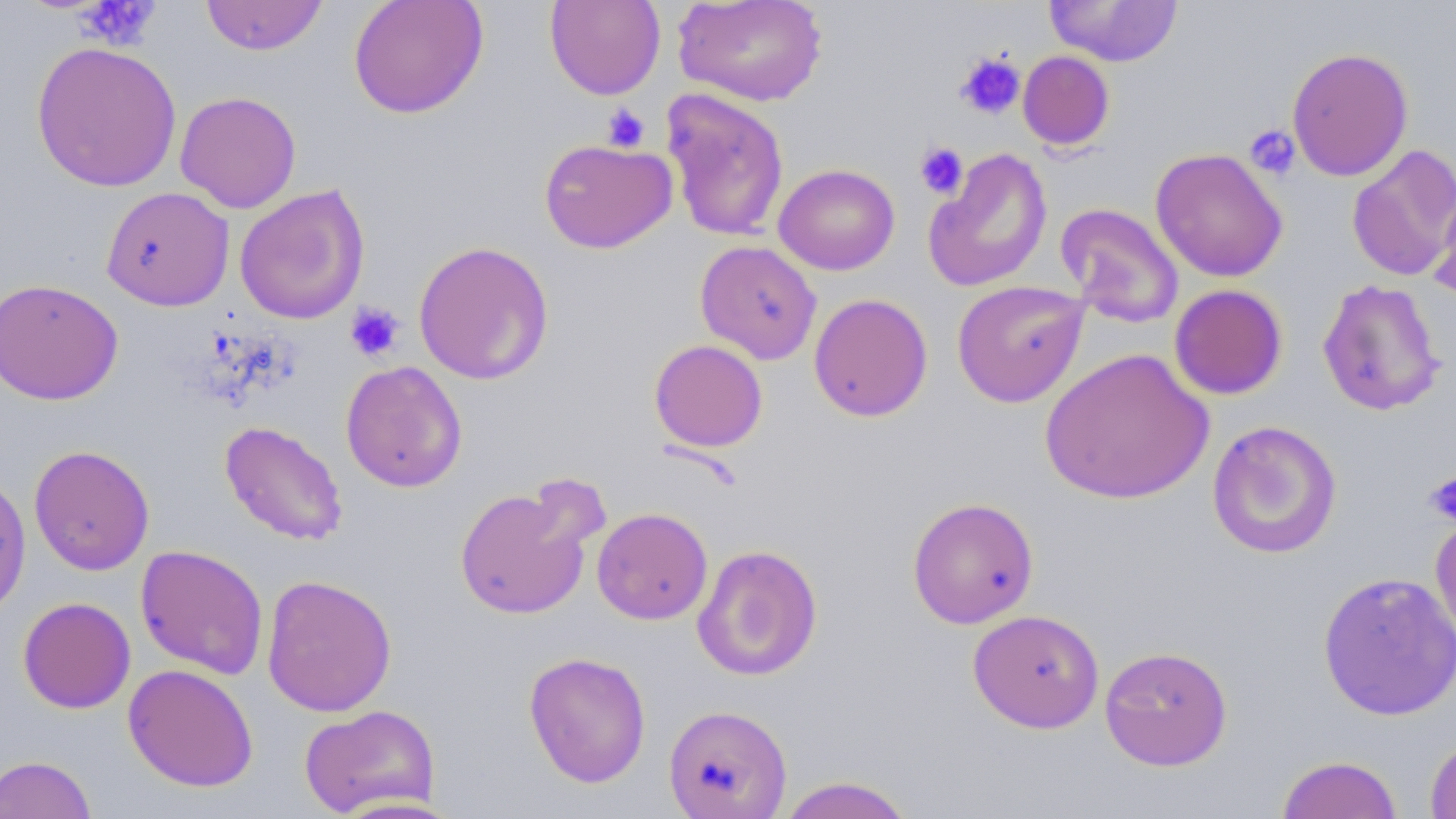

Approximate bounding boxes as (x1, y1, x2, y2) in pixels. Platelet locations: (74, 0, 161, 50), (954, 51, 1025, 120), (601, 103, 650, 152), (1244, 125, 1301, 180), (914, 142, 968, 199), (344, 302, 405, 363), (1423, 472, 1456, 525). Uninfected red blood cell locations: (201, 0, 328, 56), (348, 0, 488, 119), (544, 0, 666, 100), (673, 0, 827, 107), (1044, 0, 1183, 67), (31, 41, 182, 193), (1286, 46, 1414, 182), (1017, 50, 1115, 151), (661, 88, 790, 242), (174, 91, 302, 213), (539, 138, 677, 254), (1346, 144, 1456, 282), (922, 147, 1053, 294), (1149, 148, 1288, 282), (773, 163, 900, 275), (1429, 183, 1456, 303), (234, 184, 370, 325), (101, 186, 235, 312), (1055, 203, 1184, 328), (413, 240, 555, 385), (695, 240, 822, 364), (0, 278, 124, 404), (1317, 278, 1446, 417), (951, 280, 1089, 408), (1169, 284, 1288, 400), (808, 293, 933, 422), (649, 339, 768, 453), (1039, 347, 1214, 505), (340, 360, 467, 493), (1206, 419, 1342, 559), (219, 420, 348, 546), (28, 444, 155, 575), (0, 473, 31, 620), (454, 481, 596, 621), (907, 497, 1039, 628), (592, 507, 712, 624), (1429, 511, 1456, 654), (692, 543, 823, 681), (135, 544, 269, 680), (1317, 571, 1456, 721), (261, 573, 398, 717), (17, 596, 136, 714), (967, 609, 1104, 733), (1099, 645, 1233, 770), (523, 651, 652, 788), (122, 663, 259, 792), (298, 703, 440, 817), (663, 704, 793, 818), (1424, 734, 1456, 819), (0, 754, 97, 818), (1276, 754, 1404, 818), (776, 776, 916, 819). Slide-level diagnosis: negative for blood parasites. Captured at 1000x magnification. May-Grünwald-Giemsa stain. Thin blood smear. Optical microscopy. One field of a larger specimen. Image is 1456×819 pixels.